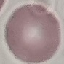
malaria status = uninfected
image type = automatically extracted cell patch, resized to 64 × 64 pixels
stain = Giemsa
preparation = thin blood film
capture = smartphone camera at the microscope eyepiece